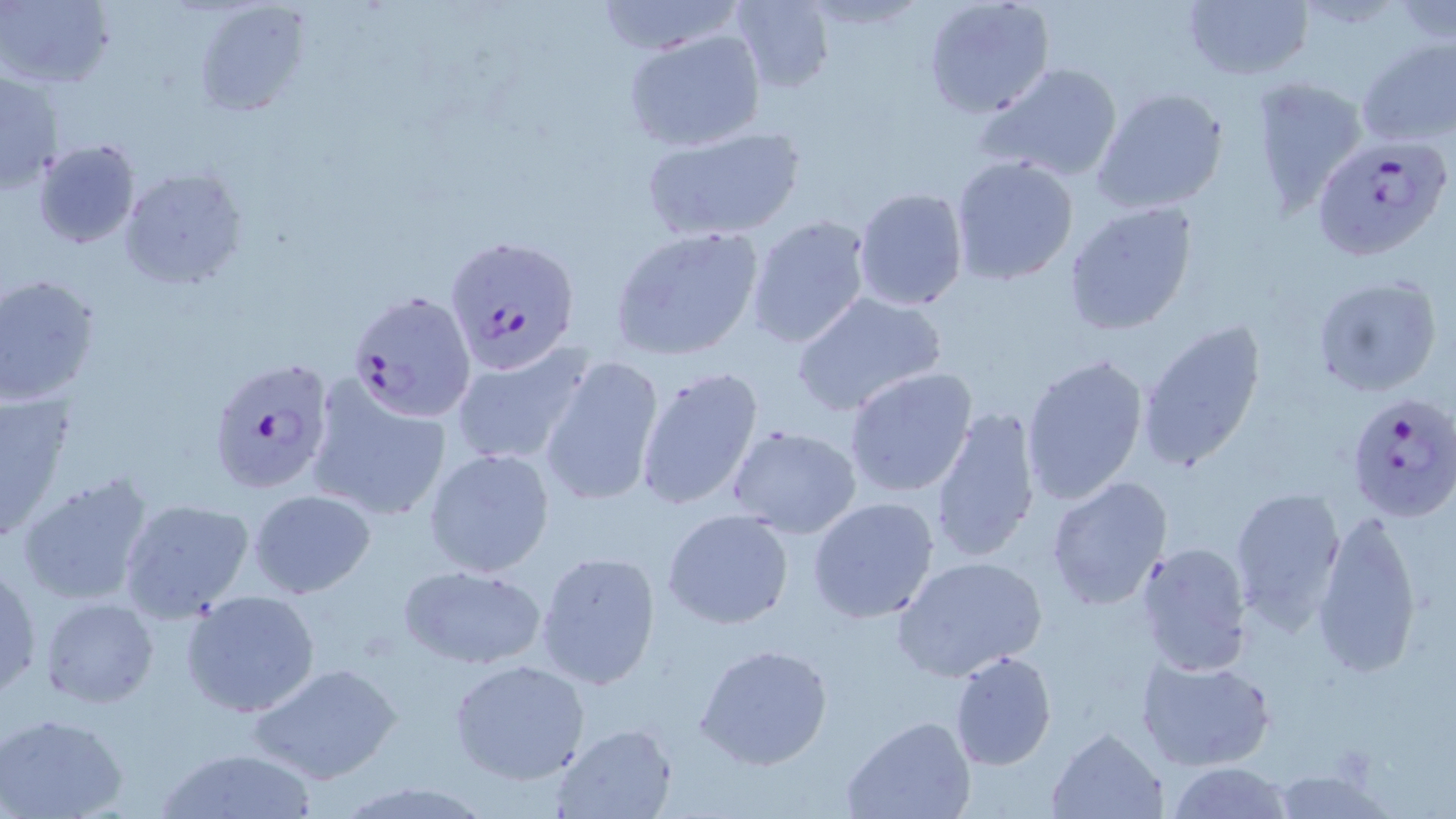

Summary:
  - Coordinate format: approximate bounding boxes as named x1/y1/x2/y2 corners in pixels
  - Plasmodium falciparum-infected red blood cell locations: (x1=1311, y1=138, x2=1449, y2=261), (x1=446, y1=235, x2=580, y2=376), (x1=348, y1=290, x2=477, y2=424), (x1=207, y1=356, x2=337, y2=495), (x1=1347, y1=393, x2=1456, y2=524)
  - Uninfected red blood cell locations: (x1=591, y1=0, x2=741, y2=56), (x1=728, y1=0, x2=836, y2=91), (x1=922, y1=0, x2=1055, y2=118), (x1=1179, y1=0, x2=1313, y2=82), (x1=1, y1=1, x2=117, y2=88), (x1=191, y1=1, x2=307, y2=119), (x1=1392, y1=2, x2=1456, y2=49), (x1=621, y1=27, x2=769, y2=153), (x1=1355, y1=37, x2=1456, y2=147), (x1=979, y1=62, x2=1124, y2=184), (x1=1, y1=66, x2=63, y2=196), (x1=1246, y1=75, x2=1369, y2=211), (x1=1088, y1=87, x2=1230, y2=215), (x1=635, y1=124, x2=808, y2=243), (x1=33, y1=139, x2=142, y2=250), (x1=949, y1=155, x2=1079, y2=287), (x1=116, y1=165, x2=251, y2=293), (x1=851, y1=186, x2=969, y2=311), (x1=1063, y1=200, x2=1198, y2=336), (x1=745, y1=213, x2=873, y2=349), (x1=609, y1=225, x2=764, y2=363), (x1=0, y1=274, x2=103, y2=406), (x1=1310, y1=274, x2=1443, y2=398), (x1=792, y1=290, x2=948, y2=418), (x1=1137, y1=317, x2=1268, y2=475), (x1=450, y1=342, x2=593, y2=468), (x1=1020, y1=353, x2=1149, y2=506), (x1=540, y1=354, x2=666, y2=508), (x1=635, y1=364, x2=766, y2=513), (x1=843, y1=367, x2=980, y2=499), (x1=305, y1=375, x2=451, y2=522), (x1=0, y1=389, x2=77, y2=540), (x1=929, y1=406, x2=1044, y2=563), (x1=725, y1=425, x2=862, y2=535), (x1=424, y1=448, x2=556, y2=578), (x1=17, y1=472, x2=154, y2=604), (x1=1045, y1=476, x2=1173, y2=612), (x1=1228, y1=487, x2=1346, y2=626), (x1=249, y1=489, x2=377, y2=600), (x1=117, y1=497, x2=255, y2=621), (x1=806, y1=497, x2=942, y2=625), (x1=1312, y1=506, x2=1424, y2=678), (x1=661, y1=508, x2=795, y2=630), (x1=1133, y1=541, x2=1253, y2=677), (x1=534, y1=551, x2=663, y2=691), (x1=894, y1=556, x2=1047, y2=683), (x1=0, y1=561, x2=41, y2=698), (x1=396, y1=563, x2=549, y2=671), (x1=181, y1=591, x2=321, y2=719), (x1=42, y1=597, x2=159, y2=707), (x1=694, y1=641, x2=834, y2=772), (x1=948, y1=649, x2=1058, y2=771), (x1=1133, y1=655, x2=1279, y2=771), (x1=449, y1=659, x2=591, y2=785), (x1=246, y1=662, x2=402, y2=787), (x1=0, y1=713, x2=129, y2=819), (x1=842, y1=716, x2=975, y2=819), (x1=551, y1=724, x2=677, y2=819), (x1=1047, y1=727, x2=1166, y2=818), (x1=151, y1=746, x2=322, y2=818), (x1=1165, y1=761, x2=1296, y2=818), (x1=1266, y1=764, x2=1393, y2=818)
  - Slide-level diagnosis: Plasmodium falciparum
  - Preparation: thin blood smear
  - Modality: optical microscopy
  - Image size: 1456×819 pixels
  - Field of view: one of a larger specimen
  - Magnification: 1000x
  - Stain: May-Grünwald-Giemsa